Outline each blood parasite and name the species.
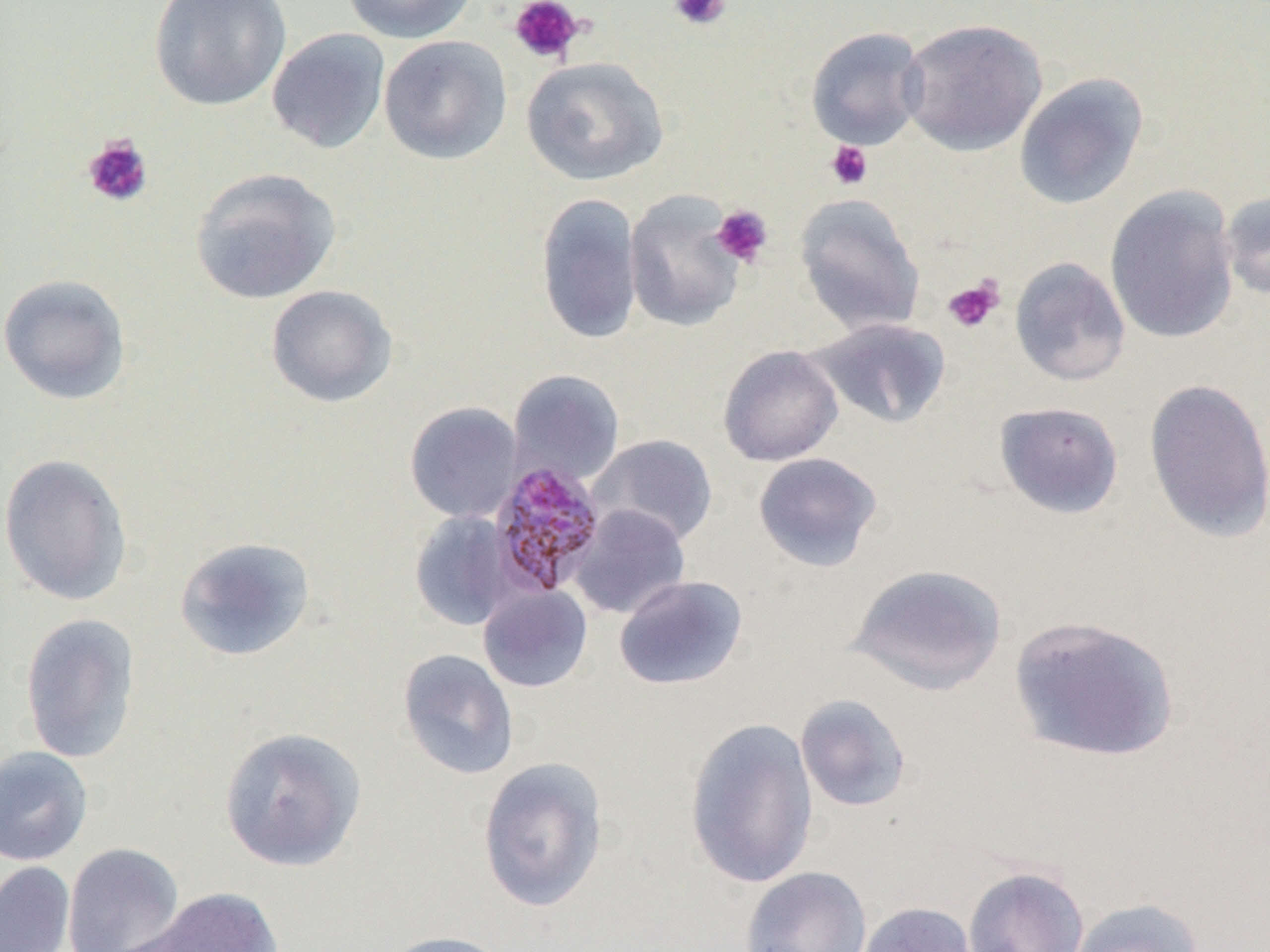
Approximate bounding boxes as [x1, y1, x2, y2] in pixels.
Plasmodium malariae-infected red blood cells: [487, 460, 607, 599].
No Plasmodium falciparum, Plasmodium ovale, Plasmodium vivax, Babesia divergens, or Trypanosoma brucei observed.

Uninfected red blood cell locations: [149, 0, 291, 111], [342, 0, 477, 44], [899, 18, 1047, 156], [805, 26, 928, 150], [266, 28, 390, 154], [379, 35, 512, 165], [521, 56, 669, 186], [1014, 72, 1149, 210], [189, 167, 341, 304], [1104, 185, 1240, 345], [1219, 190, 1270, 302], [624, 191, 746, 332], [535, 193, 643, 346], [794, 193, 926, 336], [1010, 257, 1130, 386], [0, 273, 132, 405], [266, 285, 398, 408], [805, 317, 951, 430], [718, 345, 843, 466], [507, 369, 625, 485], [1144, 378, 1270, 543], [404, 401, 523, 523], [994, 401, 1124, 519], [588, 434, 718, 547], [752, 451, 883, 572], [0, 452, 134, 607], [568, 505, 691, 619], [409, 511, 517, 631], [174, 536, 316, 662], [847, 563, 1007, 696], [614, 575, 747, 690], [478, 584, 593, 692], [20, 612, 140, 764], [1008, 614, 1180, 763], [397, 648, 520, 781], [795, 694, 912, 812], [685, 717, 819, 889], [219, 726, 366, 872], [0, 746, 94, 866], [476, 757, 609, 912], [62, 842, 185, 952], [0, 861, 75, 952], [739, 865, 872, 952], [962, 865, 1089, 952], [133, 886, 286, 951], [1067, 897, 1204, 952], [856, 901, 979, 952], [379, 930, 510, 952]. Platelet locations: [508, 0, 584, 65], [668, 0, 731, 32], [82, 135, 153, 207], [825, 141, 873, 190], [710, 205, 773, 268], [942, 276, 1005, 333]. Slide-level diagnosis: Plasmodium malariae. 1000x magnification. Optical microscopy. Thin blood smear. Image is 1270×952 pixels. One field of a larger specimen.